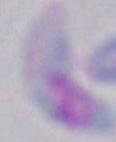
identification = Toxoplasma gondii
modality = micrograph
magnification = 1000x